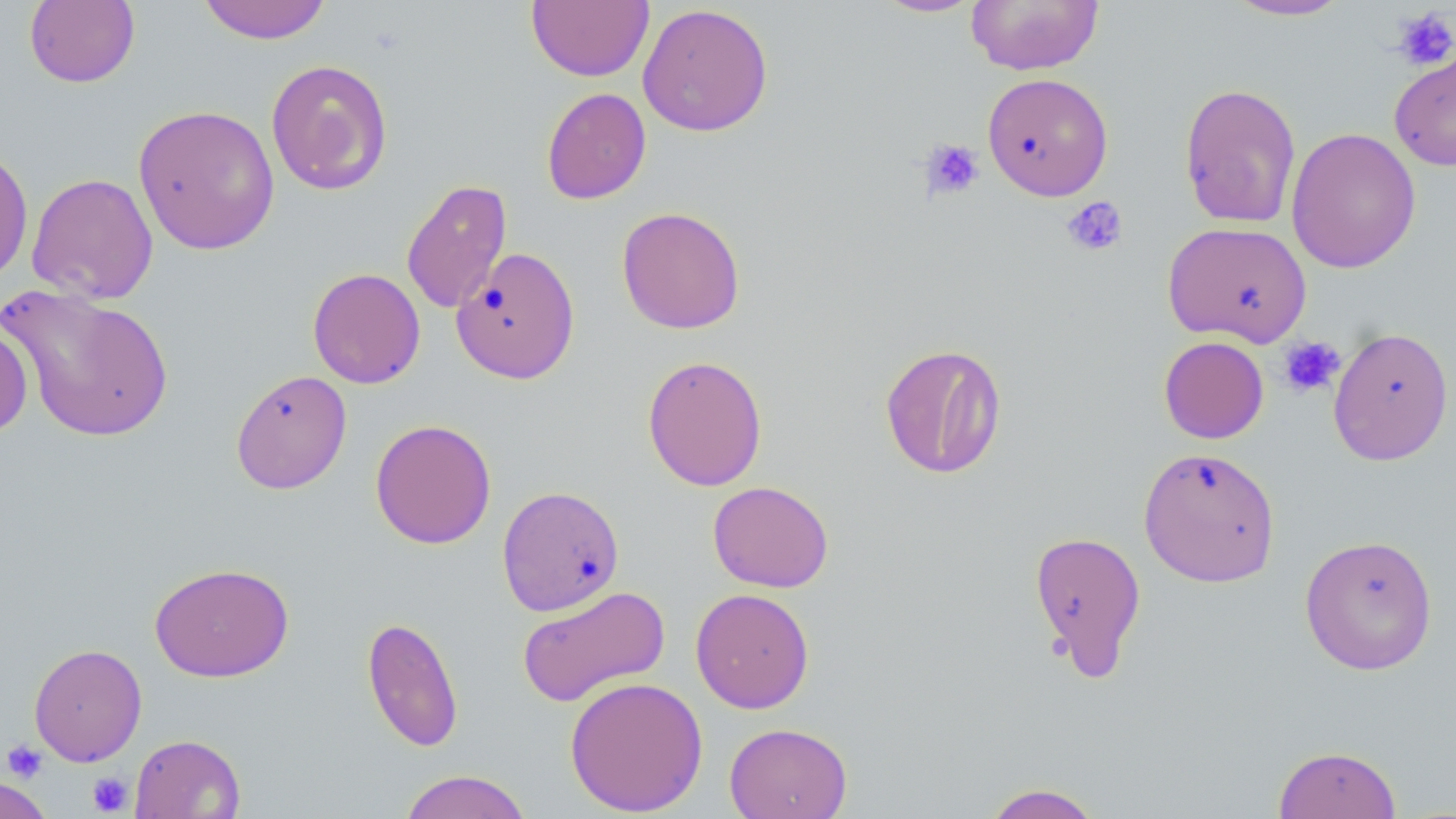

Approximate bounding boxes as (x1, y1, x2, y2) in pixels. Platelet locations: (1391, 7, 1456, 72), (919, 138, 985, 200), (1062, 196, 1128, 257), (1278, 336, 1345, 398), (2, 740, 48, 782), (87, 772, 133, 815). Uninfected red blood cell locations: (198, 0, 331, 44), (966, 0, 1104, 75), (24, 1, 140, 88), (526, 1, 653, 82), (872, 1, 986, 18), (1224, 1, 1352, 21), (637, 3, 774, 137), (1389, 45, 1456, 172), (265, 59, 394, 196), (982, 73, 1114, 200), (1179, 82, 1302, 229), (541, 87, 651, 204), (133, 103, 280, 255), (1286, 127, 1422, 274), (0, 144, 34, 286), (26, 172, 158, 305), (401, 178, 512, 315), (616, 206, 746, 334), (1162, 221, 1312, 347), (451, 246, 581, 385), (307, 267, 426, 389), (1, 284, 175, 443), (0, 323, 33, 438), (1328, 326, 1454, 465), (1158, 336, 1269, 443), (879, 343, 1007, 479), (642, 354, 768, 492), (230, 369, 352, 494), (370, 418, 496, 549), (1138, 446, 1281, 588), (707, 480, 834, 592), (497, 485, 624, 616), (1027, 530, 1148, 679), (1299, 533, 1438, 675), (149, 562, 294, 682), (516, 584, 670, 708), (690, 588, 815, 713), (361, 616, 464, 752), (28, 643, 147, 766), (565, 676, 708, 816), (724, 722, 853, 819), (129, 733, 246, 819), (1272, 745, 1401, 819), (398, 769, 533, 819), (0, 775, 54, 819), (980, 783, 1105, 819). Slide-level diagnosis: no evidence of blood parasites. Light microscopy. Thin blood film. Single field of view. Image is 1456×819 pixels. May-Grünwald-Giemsa stain. Captured at 1000x magnification.